Give the position of every leukocyte visible.
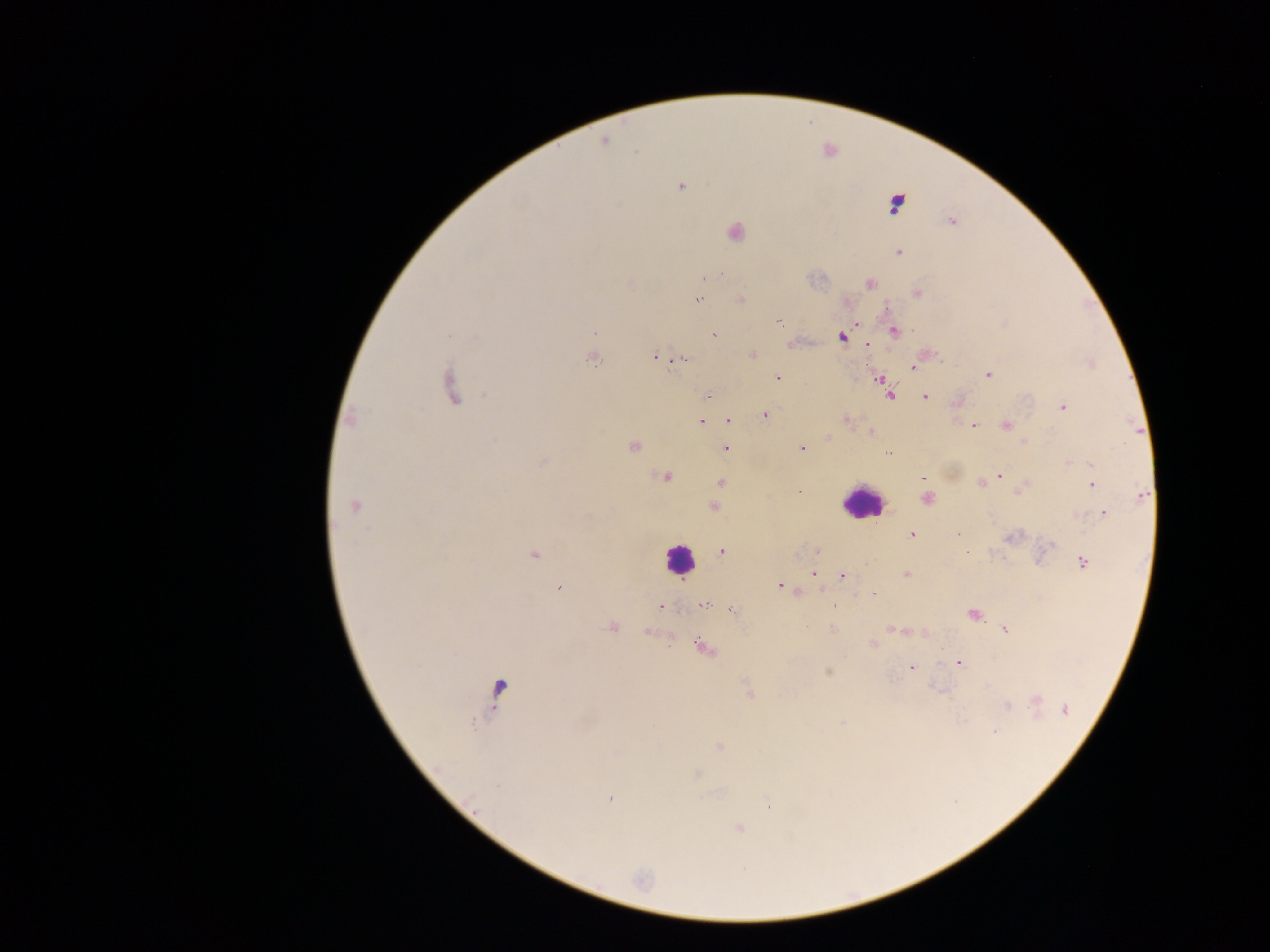
Approximate centers as {x, y} in pixels.
Leukocytes: {860, 502}, {679, 558}.

Plasmodium parasite locations: {605, 141}, {681, 187}, {897, 204}, {951, 221}, {735, 233}, {899, 252}, {870, 283}, {918, 293}, {741, 299}, {697, 300}, {778, 322}, {856, 323}, {894, 331}, {595, 332}, {714, 335}, {842, 337}, {867, 346}, {751, 355}, {655, 356}, {682, 358}, {593, 359}, {1092, 363}, {913, 367}, {988, 374}, {778, 378}, {879, 379}, {884, 387}, {454, 388}, {890, 395}, {708, 397}, {925, 397}, {957, 403}, {1063, 407}, {764, 415}, {350, 419}, {845, 420}, {729, 421}, {700, 422}, {1005, 426}, {974, 427}, {871, 432}, {828, 437}, {633, 447}, {725, 448}, {801, 449}, {888, 452}, {543, 462}, {1068, 462}, {1091, 464}, {998, 475}, {665, 477}, {923, 477}, {986, 480}, {720, 482}, {980, 482}, {1092, 485}, {1022, 489}, {1142, 495}, {926, 499}, {354, 506}, {713, 507}, {1103, 514}, {1075, 516}, {959, 534}, {912, 535}, {1012, 536}, {1046, 548}, {817, 550}, {722, 551}, {965, 552}, {534, 555}, {1084, 563}, {814, 573}, {907, 574}, {842, 577}, {781, 586}, {559, 588}, {874, 594}, {704, 605}, {661, 607}, {733, 611}, {973, 615}, {612, 626}, {832, 628}, {891, 629}, {1005, 630}, {872, 643}, {705, 648}, {959, 663}, {911, 667}, {828, 672}, {497, 691}, {749, 691}, {1037, 701}, {1006, 705}, {1065, 710}, {843, 723}, {994, 732}, {718, 746}, {616, 752}, {695, 775}, {498, 786}, {611, 798}, {769, 805}, {739, 829}, {642, 880}. Collected in Ghana. Single field of view. Image is 1270×952 pixels. Thick blood smear. Photographed through a microscope with a mobile-phone camera.